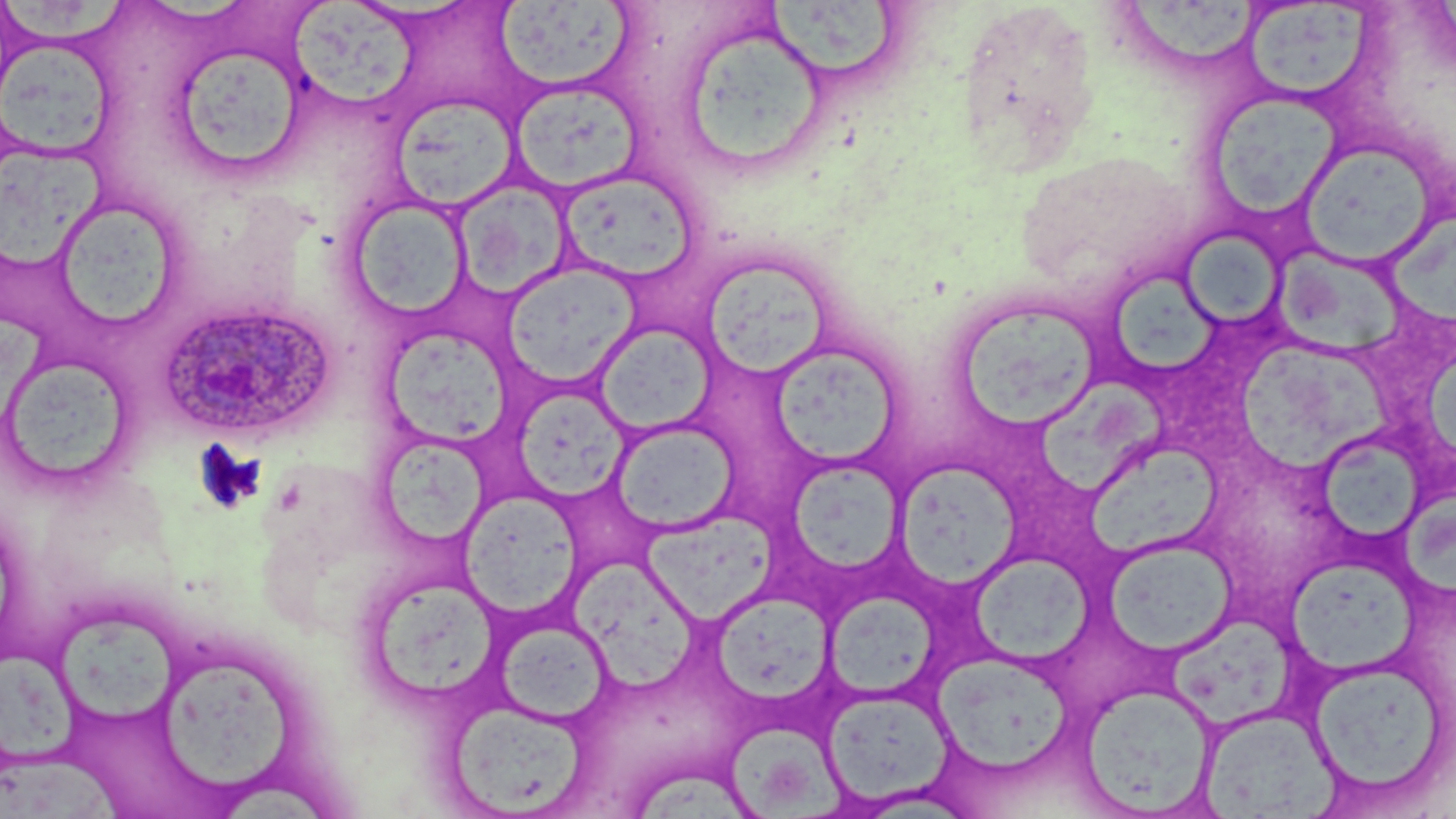

slide_level_diagnosis: Plasmodium ovale
preparation: thin blood film
image_size: 1456×819 pixels
field_of_view: single
magnification: 1000x
modality: optical microscopy
stain: May-Grünwald-Giemsa
uninfected_red_blood_cell_locations: 'approximate bounding boxes as (x1,y1)-(x2,y2) corner pairs in pixels: (764,0)-(897,77), (288,1)-(420,109), (494,1)-(635,91), (0,2)-(137,45), (956,2)-(1102,173), (1122,2)-(1263,61), (1239,2)-(1376,102), (681,33)-(822,168), (0,39)-(116,159), (170,44)-(309,178), (511,78)-(644,193), (1202,90)-(1346,225), (397,97)-(516,212), (1297,139)-(1439,268), (0,144)-(115,274), (1016,152)-(1191,293), (556,168)-(700,284), (453,181)-(571,297), (49,196)-(186,332), (348,198)-(472,322), (1389,202)-(1456,326), (1178,229)-(1286,329), (1274,251)-(1409,363), (699,256)-(832,379), (505,266)-(638,385), (1117,277)-(1224,373), (949,297)-(1103,434), (384,323)-(512,445), (595,324)-(717,436), (776,344)-(897,464), (1237,344)-(1405,473), (0,352)-(140,493), (1039,376)-(1176,494), (513,386)-(629,503), (611,419)-(739,535), (1317,442)-(1429,544), (386,443)-(493,545), (1091,443)-(1225,556), (790,456)-(902,573), (897,460)-(1024,596), (1400,490)-(1456,603), (460,495)-(583,621), (642,514)-(782,631), (1105,539)-(1236,657), (972,554)-(1092,665), (1288,556)-(1428,674), (571,566)-(698,695), (364,574)-(501,709), (826,592)-(938,703), (715,597)-(839,699), (56,611)-(181,723), (1158,616)-(1304,729), (496,617)-(612,725), (0,644)-(83,766), (934,653)-(1072,773), (158,659)-(296,789), (1309,660)-(1448,798), (1081,684)-(1217,814), (826,689)-(950,804), (446,701)-(590,815), (1201,707)-(1337,817), (735,725)-(847,819), (1,757)-(129,819), (637,770)-(756,819)'
plasmodium_ovale_infected_red_blood_cell_locations: 'approximate bounding boxes as (x1,y1)-(x2,y2) corner pairs in pixels: (158,299)-(337,442)'